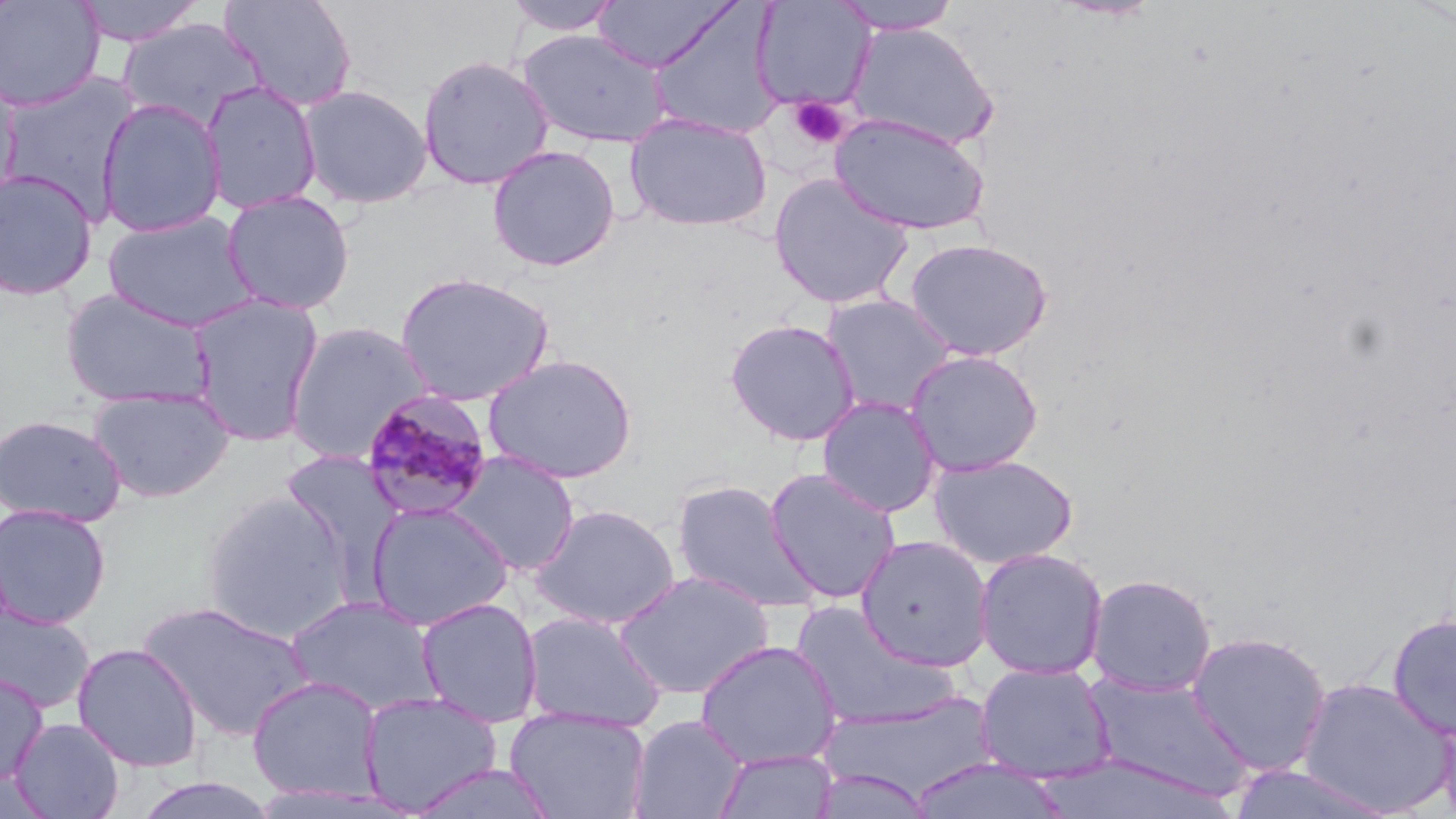

Summary:
  - Coordinate format: approximate bounding boxes as (x1,y1)-(x2,y2) corner pairs in pixels
  - Platelet locations: (789,96)-(849,150)
  - Uninfected red blood cell locations: (0,0)-(105,112), (72,0)-(205,47), (218,0)-(358,112), (502,0)-(624,37), (592,0)-(738,72), (750,0)-(875,114), (831,0)-(964,35), (648,4)-(787,139), (117,17)-(268,133), (846,22)-(1000,151), (518,28)-(672,148), (417,54)-(555,190), (0,70)-(144,216), (0,71)-(23,208), (200,80)-(323,215), (297,84)-(433,209), (95,98)-(227,238), (624,112)-(772,233), (829,113)-(991,236), (486,144)-(621,272), (0,168)-(99,301), (767,172)-(915,310), (221,190)-(356,315), (103,209)-(259,332), (903,237)-(1054,362), (394,271)-(555,407), (60,287)-(217,410), (187,293)-(324,448), (821,293)-(959,418), (725,318)-(861,446), (284,322)-(433,464), (903,348)-(1044,476), (481,353)-(639,484), (88,386)-(235,503), (816,395)-(942,517), (0,415)-(126,528), (280,449)-(406,584), (449,451)-(579,576), (927,453)-(1079,569), (764,467)-(902,604), (670,478)-(820,614), (200,490)-(355,643), (365,500)-(514,631), (0,502)-(112,628), (529,502)-(681,630), (856,534)-(994,672), (974,547)-(1109,680), (612,570)-(776,700), (1085,572)-(1218,696), (284,595)-(445,717), (414,597)-(544,727), (136,600)-(316,741), (789,600)-(956,729), (0,603)-(95,713), (520,609)-(667,732), (1386,612)-(1456,740), (1187,630)-(1332,776), (694,639)-(842,770), (71,642)-(204,772), (974,661)-(1117,784), (0,670)-(48,787), (1081,670)-(1253,801), (246,675)-(385,803), (1295,676)-(1454,816), (357,691)-(503,815), (822,693)-(999,800), (506,707)-(651,819), (628,714)-(748,819), (8,717)-(125,818), (711,748)-(841,819), (907,758)-(1071,819), (404,763)-(562,819), (1225,764)-(1398,819), (808,768)-(938,819), (129,775)-(284,819)
  - Plasmodium malariae-infected red blood cell locations: (359,388)-(496,522)
  - Slide-level diagnosis: Plasmodium malariae
  - Modality: light microscopy
  - Preparation: thin blood smear
  - Image size: 1456×819 pixels
  - Magnification: 1000x
  - Stain: May-Grünwald-Giemsa
  - Field of view: single